Describe the morphology of the erythrocytes.
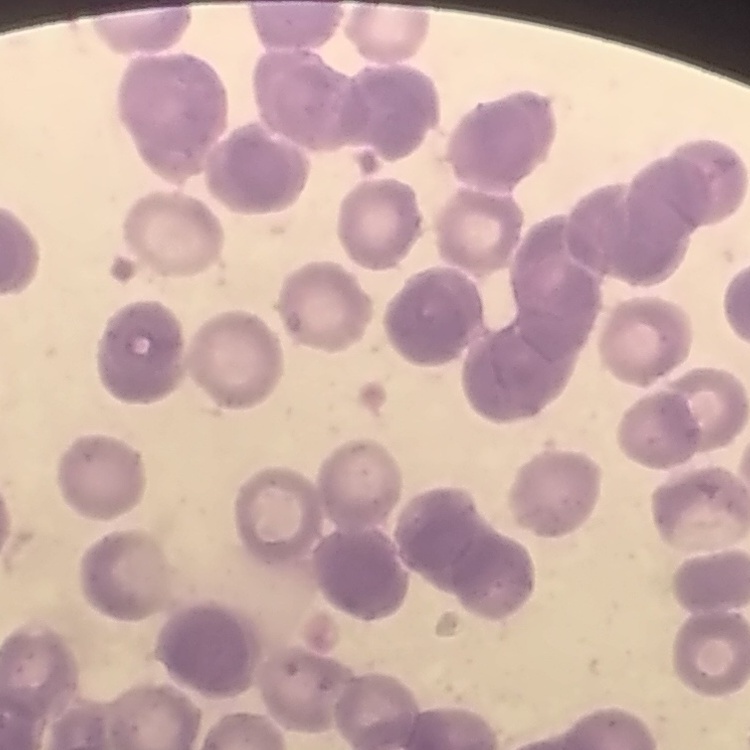

They show rouleaux formation.

Thin blood film. Square crop of a larger photomicrograph. Stained with either Field's or Giemsa.